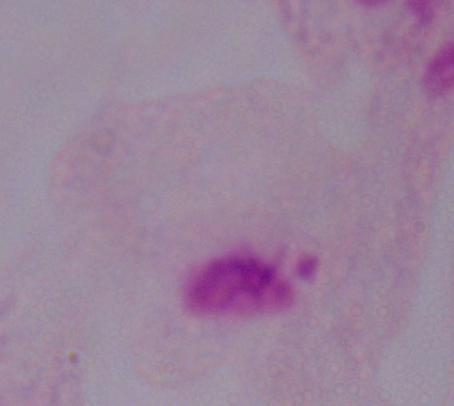

A trichomonad is shown. Captured at 1000x magnification. Photomicrograph.